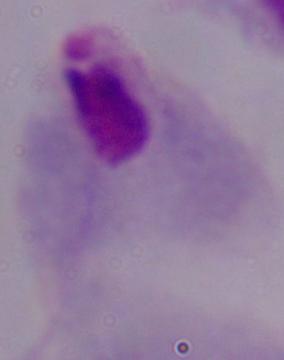

modality: photomicrograph
magnification: 1000x
identification: trichomonad